Classify this cell by malaria status.
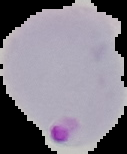

Parasitized.

Summary:
  - Image size: 127×154 pixels
  - Preparation: thin blood smear
  - Image type: segmented cell region with the area outside set to black